Report the malaria status of this cell.
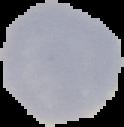
Uninfected.

Cell region segmented out of the field of view; the surrounding area is masked to black. From a thin blood film. Image is 124×127 pixels.